Give the position of every Plasmodium parasite visible.
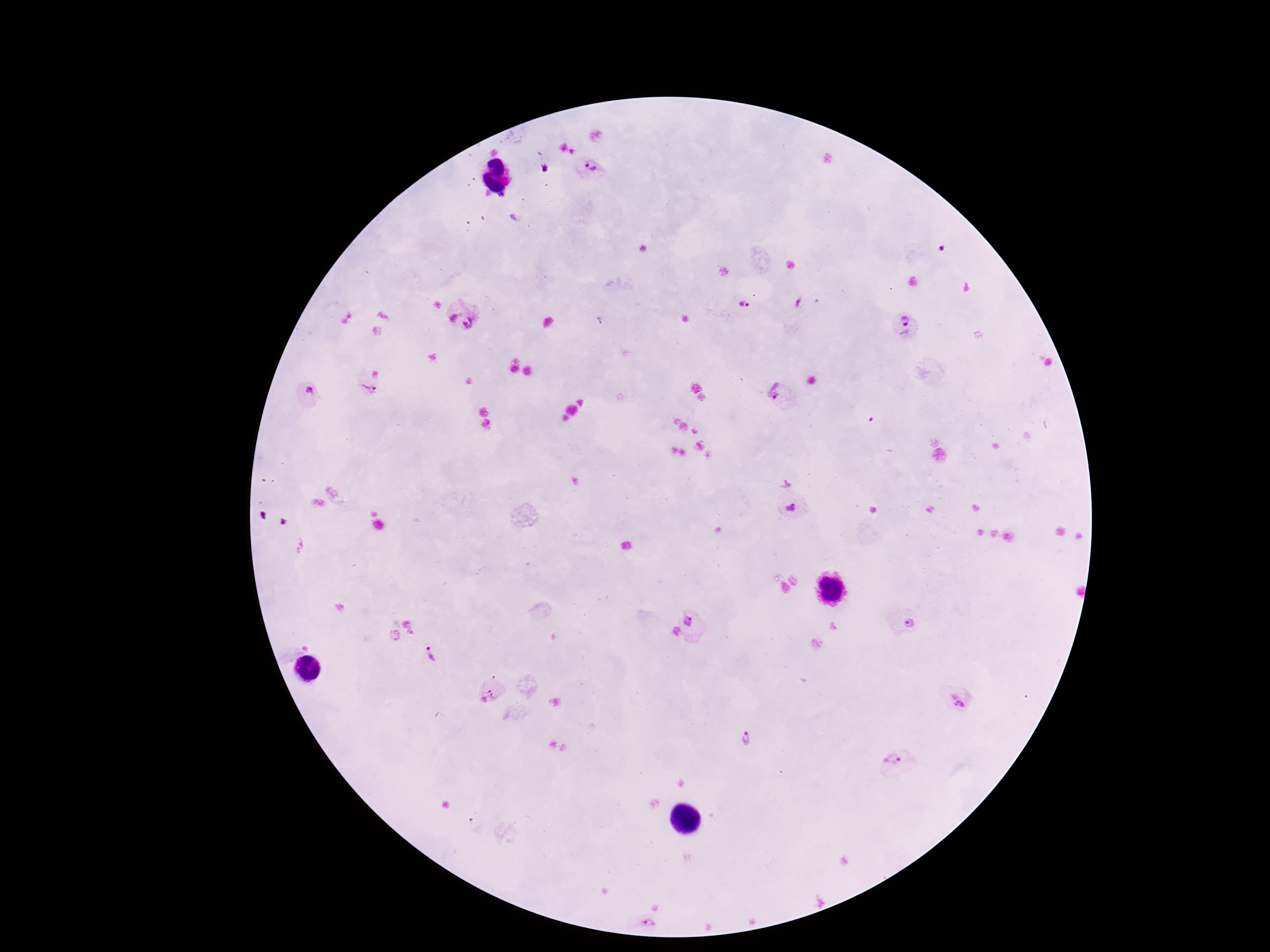
Approximate centers as (x, y) in pixels.
Plasmodium parasites: (592, 167), (747, 303), (462, 314), (905, 325), (371, 385), (307, 393), (782, 396), (792, 507), (693, 620), (907, 622), (428, 655), (491, 692), (957, 697), (748, 740), (896, 760), (646, 920).

Summary:
  - Magnification: 100x
  - Stain: Giemsa
  - Preparation: thick blood film
  - Capture: smartphone camera through the microscope eyepiece
  - Image size: 1270×952 pixels
  - Field of view: one from this slide
  - Patient malaria status: infected